Comment on the morphology of the erythrocytes.
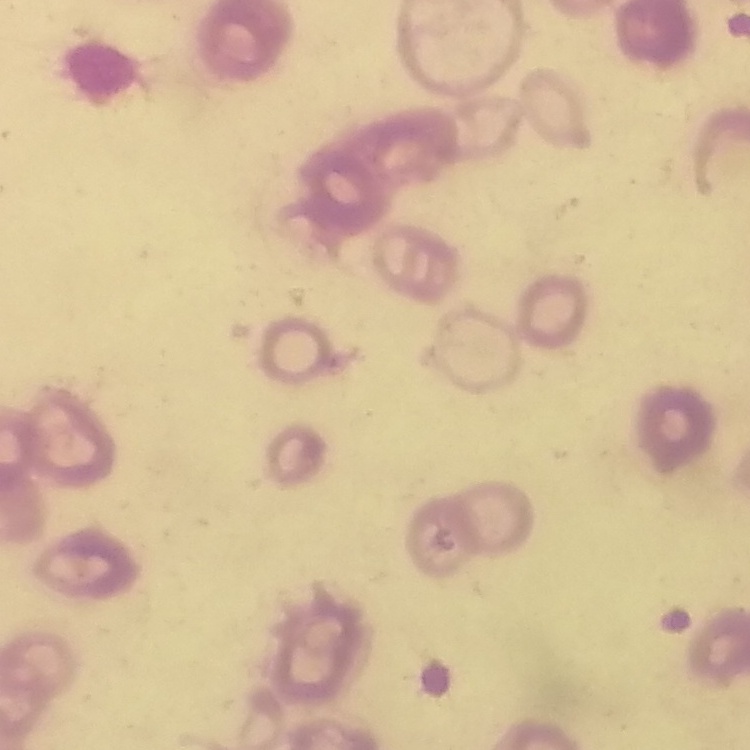

They show rouleaux formation.

{
  "stain": "Field's or Giemsa",
  "preparation": "thin peripheral smear",
  "image_type": "one tile cut from a larger photomicrograph"
}